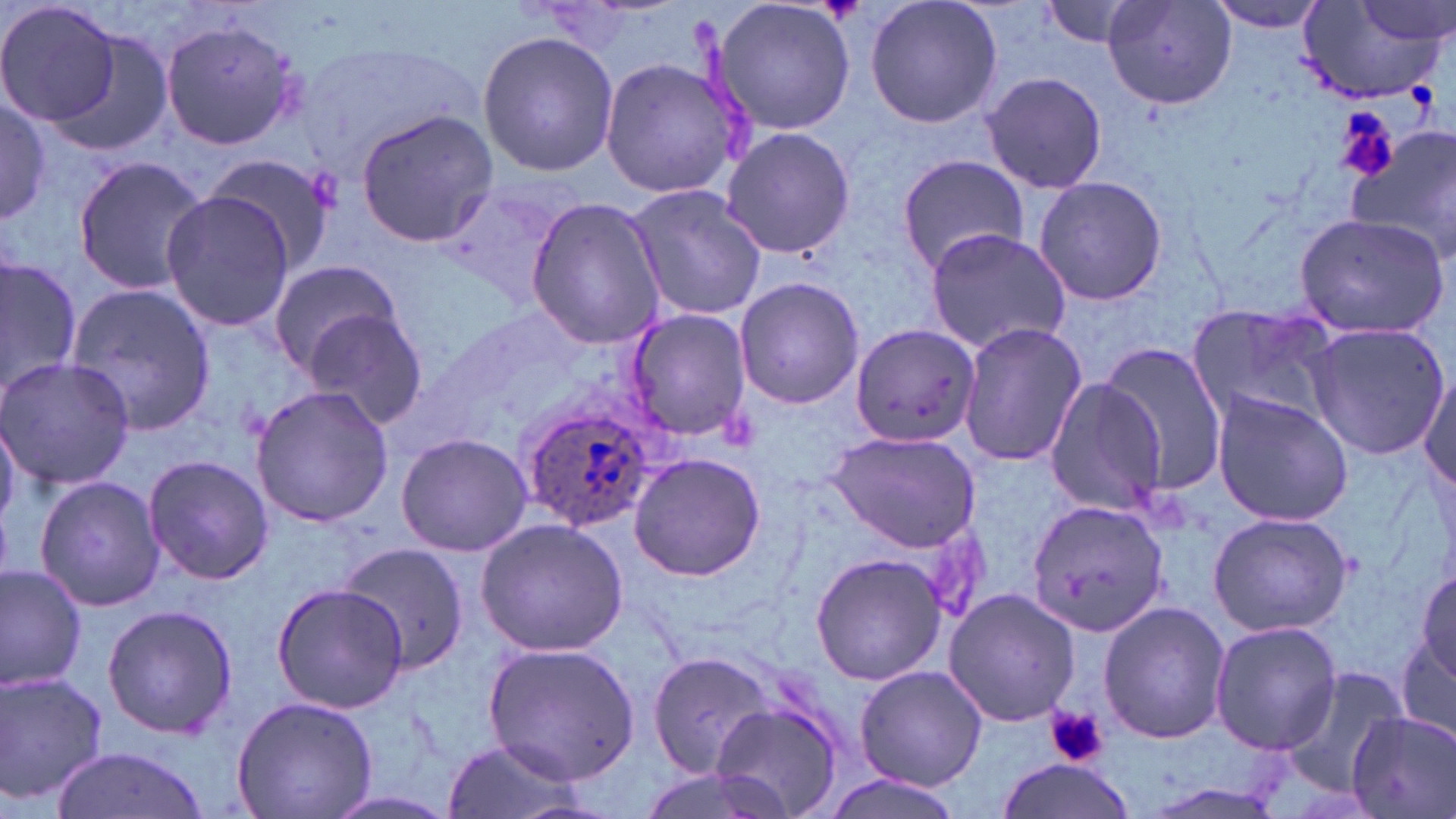

slide_level_diagnosis: Plasmodium ovale
field_of_view: one of a larger specimen
image_size: 1456×819 pixels
preparation: thin blood smear
uninfected_red_blood_cell_locations: 'approximate bounding boxes as (x1, y1, x2, y2) in pixels: (0, 0, 121, 129), (711, 0, 857, 137), (865, 0, 1001, 129), (1201, 0, 1332, 33), (1040, 1, 1150, 50), (1103, 1, 1238, 111), (1297, 1, 1450, 104), (1355, 1, 1453, 46), (161, 20, 303, 150), (49, 25, 176, 160), (478, 31, 621, 177), (597, 53, 746, 201), (982, 71, 1109, 195), (0, 95, 51, 224), (355, 110, 497, 247), (719, 125, 854, 261), (1345, 130, 1455, 261), (205, 151, 337, 277), (897, 152, 1028, 279), (71, 155, 209, 294), (1032, 175, 1169, 307), (625, 184, 768, 320), (159, 190, 297, 331), (524, 196, 665, 348), (1293, 211, 1448, 339), (921, 227, 1072, 354), (0, 255, 80, 403), (266, 257, 405, 376), (733, 276, 864, 410), (65, 282, 217, 439), (1186, 301, 1345, 430), (302, 305, 434, 432), (624, 307, 753, 441), (957, 321, 1087, 468), (1303, 321, 1450, 461), (852, 323, 982, 448), (1096, 343, 1230, 493), (0, 356, 133, 490), (1418, 365, 1454, 500), (1042, 374, 1171, 515), (252, 382, 392, 528), (1211, 391, 1353, 526), (828, 430, 984, 553), (394, 431, 533, 558), (142, 454, 273, 586), (628, 454, 768, 581), (33, 474, 166, 612), (1026, 500, 1172, 638), (1207, 510, 1355, 640), (475, 517, 630, 656), (337, 542, 473, 673), (809, 553, 948, 686), (1413, 560, 1454, 692), (0, 562, 87, 690), (269, 581, 410, 714), (942, 588, 1080, 726), (1098, 599, 1230, 745), (100, 603, 237, 741), (1395, 608, 1454, 758), (1210, 620, 1342, 756), (482, 642, 637, 780), (646, 648, 778, 778), (854, 665, 988, 790), (1275, 667, 1405, 795), (0, 668, 109, 808), (229, 694, 376, 819), (709, 699, 844, 819), (1346, 711, 1456, 819), (438, 734, 598, 819), (50, 745, 209, 819), (996, 758, 1137, 819), (815, 773, 970, 818), (1137, 780, 1291, 818)'
magnification: 1000x
plasmodium_ovale_infected_red_blood_cell_locations: 'approximate bounding boxes as (x1, y1, x2, y2) in pixels: (516, 398, 666, 531)'
modality: light microscopy
platelet_locations: 'approximate bounding boxes as (x1, y1, x2, y2) in pixels: (1336, 108, 1399, 182), (1047, 705, 1107, 768)'
stain: May-Grünwald-Giemsa